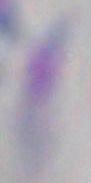 Micrograph. Captured at 1000x magnification. Toxoplasma gondii is seen.